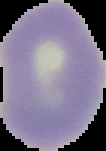
Summary:
  - Image type: cell region segmented out of the field of view; surrounding area masked to black
  - Image size: 106×151 pixels
  - Result: negative for malaria parasites
  - Preparation: thin blood smear